Name the blood parasite species.
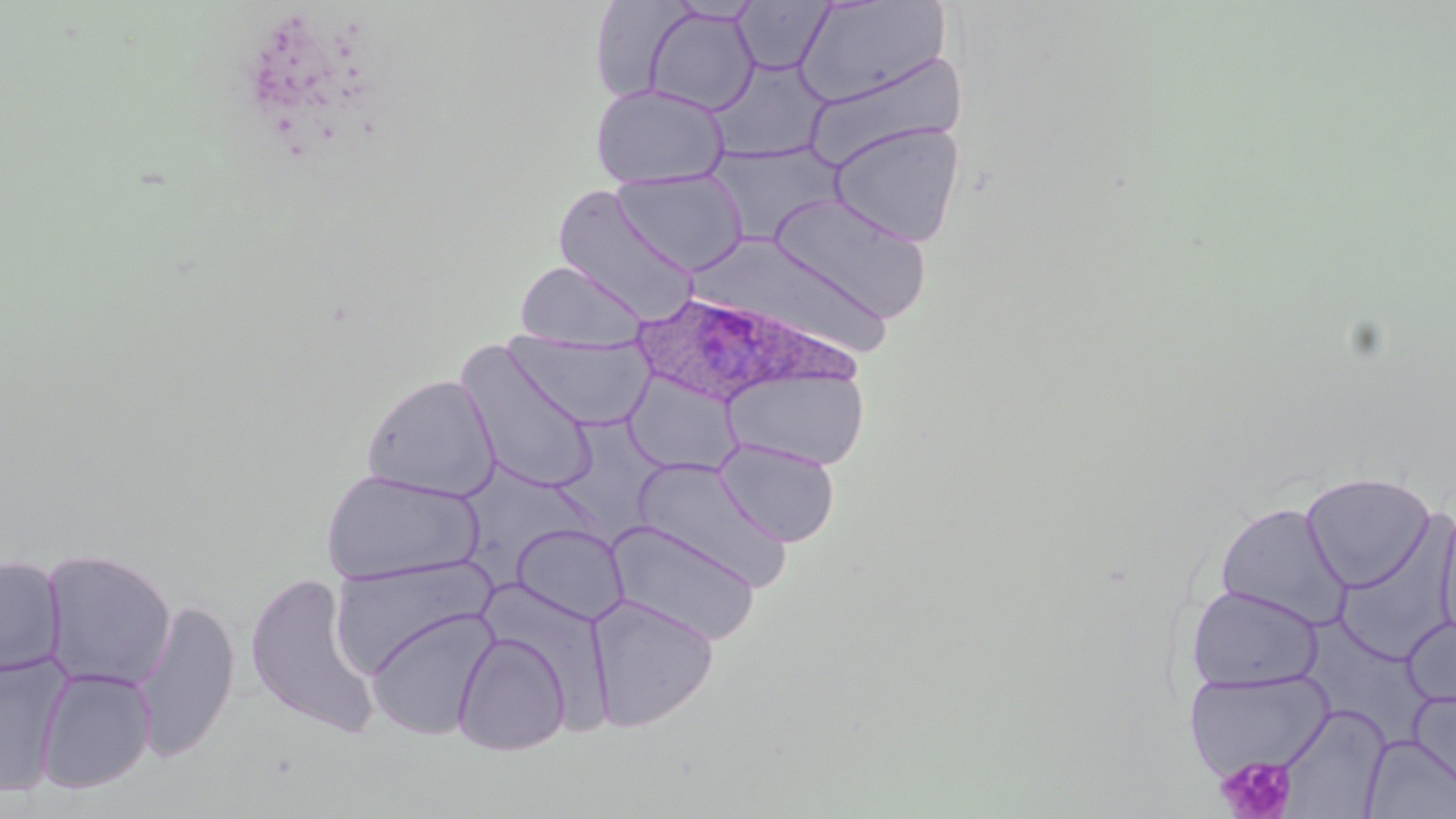

Plasmodium ovale.

platelet locations = approximate bounding boxes as (x1, y1, x2, y2) in pixels: (1216, 756, 1296, 819)
stain = May-Grünwald-Giemsa
field of view = one of a larger specimen
uninfected red blood cell locations = approximate bounding boxes as (x1, y1, x2, y2) in pixels: (794, 0, 950, 107), (666, 1, 763, 24), (732, 1, 835, 75), (589, 2, 696, 102), (642, 6, 760, 116), (801, 51, 968, 171), (706, 58, 831, 163), (590, 83, 730, 189), (828, 121, 966, 247), (706, 142, 843, 246), (611, 168, 749, 275), (552, 186, 701, 323), (767, 192, 933, 325), (689, 232, 896, 363), (514, 260, 649, 351), (507, 333, 654, 430), (457, 343, 600, 495), (723, 366, 870, 471), (361, 374, 500, 500), (619, 374, 746, 474), (556, 415, 673, 536), (715, 437, 841, 547), (632, 457, 792, 590), (461, 466, 591, 595), (321, 468, 484, 586), (1300, 471, 1437, 592), (1214, 501, 1351, 630), (1434, 501, 1456, 653), (1335, 507, 1456, 667), (605, 520, 761, 645), (511, 523, 629, 626), (40, 548, 177, 691), (328, 554, 497, 678), (0, 555, 66, 678), (243, 572, 381, 738), (1187, 584, 1324, 692), (586, 593, 720, 734), (132, 597, 239, 765), (364, 608, 498, 740), (1300, 615, 1430, 753), (1402, 615, 1456, 711), (453, 632, 571, 755), (0, 653, 72, 797), (34, 667, 156, 793), (1185, 668, 1336, 777), (1408, 689, 1456, 793), (1277, 705, 1390, 818), (1361, 734, 1456, 818)
image size = 1456×819 pixels
preparation = thin blood smear
modality = light microscopy
magnification = 1000x
Plasmodium ovale-infected red blood cell locations = approximate bounding boxes as (x1, y1, x2, y2) in pixels: (628, 291, 855, 406)